Name the parasite shown.
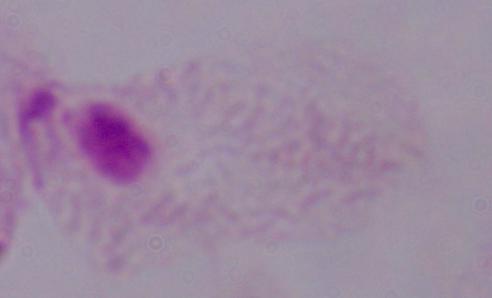

A trichomonad.

Summary:
  - Modality: micrograph
  - Magnification: 1000x